State which parasite is depicted.
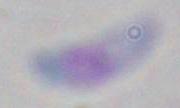

This is Toxoplasma gondii.

1000x magnification. Photomicrograph.